State the blood parasite species.
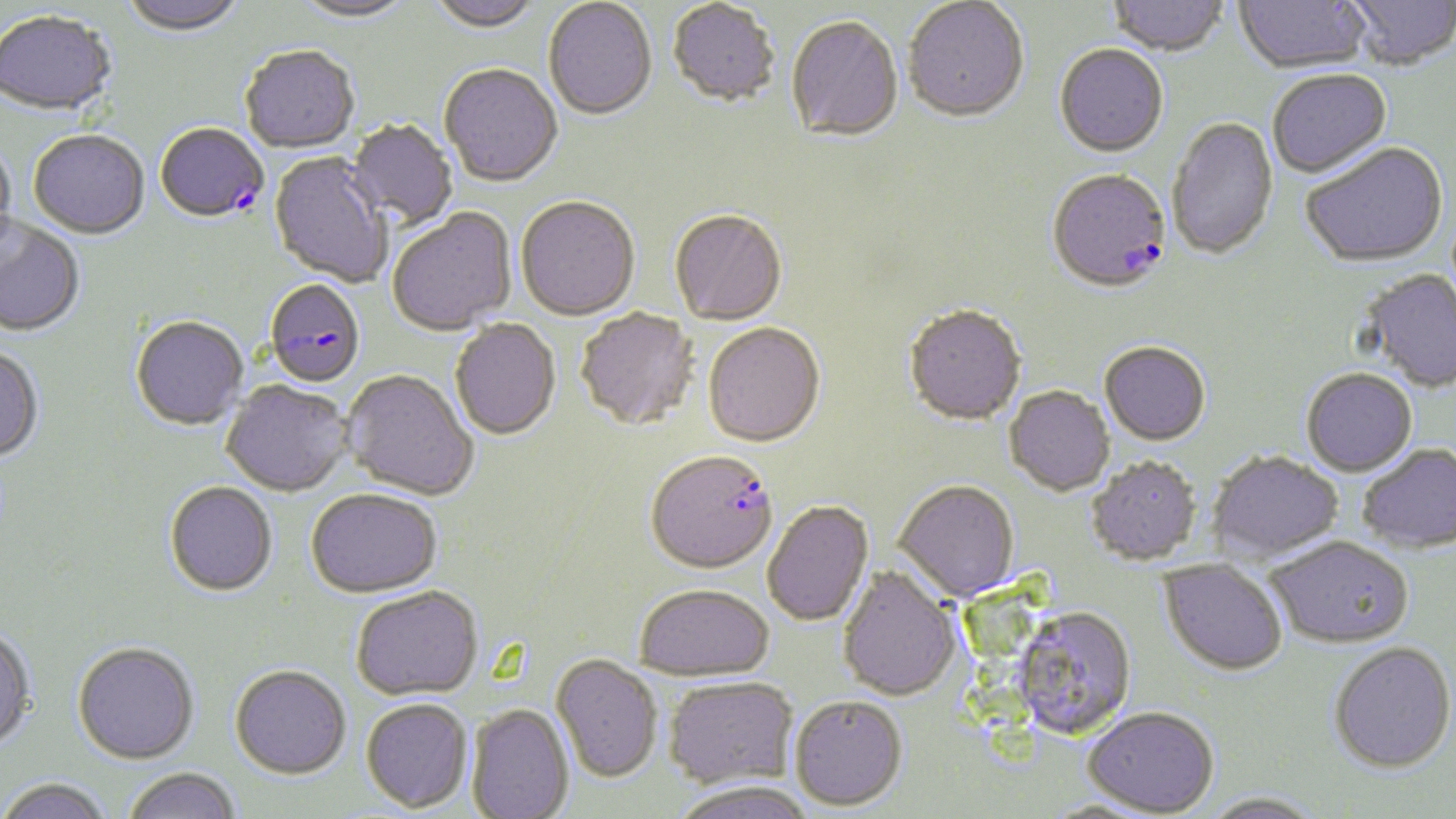
Plasmodium falciparum.

stain = May-Grünwald-Giemsa
Plasmodium falciparum-infected red blood cell locations = approximate bounding boxes as named x1/y1/x2/y2 corners in pixels: (x1=155, y1=125, x2=269, y2=225), (x1=1047, y1=171, x2=1172, y2=296), (x1=264, y1=281, x2=365, y2=389), (x1=646, y1=452, x2=779, y2=576)
magnification = 1000x
image size = 1456×819 pixels
modality = optical microscopy
preparation = thin blood smear
field of view = single
uninfected red blood cell locations = approximate bounding boxes as named x1/y1/x2/y2 corners in pixels: (x1=118, y1=0, x2=248, y2=38), (x1=291, y1=0, x2=418, y2=26), (x1=426, y1=0, x2=544, y2=36), (x1=1234, y1=0, x2=1372, y2=75), (x1=1342, y1=0, x2=1456, y2=73), (x1=543, y1=1, x2=657, y2=123), (x1=903, y1=1, x2=1029, y2=125), (x1=1107, y1=1, x2=1228, y2=58), (x1=667, y1=2, x2=780, y2=110), (x1=0, y1=13, x2=117, y2=120), (x1=786, y1=18, x2=904, y2=145), (x1=1054, y1=46, x2=1168, y2=159), (x1=240, y1=47, x2=360, y2=155), (x1=438, y1=65, x2=563, y2=189), (x1=1267, y1=71, x2=1392, y2=180), (x1=1167, y1=118, x2=1279, y2=262), (x1=347, y1=119, x2=458, y2=230), (x1=28, y1=132, x2=149, y2=241), (x1=0, y1=139, x2=17, y2=256), (x1=1301, y1=145, x2=1449, y2=270), (x1=267, y1=154, x2=392, y2=288), (x1=515, y1=198, x2=640, y2=322), (x1=388, y1=209, x2=517, y2=336), (x1=669, y1=212, x2=787, y2=327), (x1=0, y1=218, x2=85, y2=339), (x1=1360, y1=270, x2=1456, y2=393), (x1=904, y1=307, x2=1026, y2=428), (x1=575, y1=309, x2=700, y2=433), (x1=129, y1=316, x2=249, y2=431), (x1=450, y1=320, x2=561, y2=442), (x1=703, y1=324, x2=826, y2=449), (x1=1099, y1=343, x2=1211, y2=447), (x1=0, y1=347, x2=45, y2=465), (x1=1300, y1=369, x2=1418, y2=477), (x1=341, y1=371, x2=478, y2=501), (x1=221, y1=381, x2=353, y2=497), (x1=1004, y1=386, x2=1115, y2=497), (x1=1357, y1=443, x2=1456, y2=553), (x1=1207, y1=450, x2=1344, y2=563), (x1=1086, y1=457, x2=1202, y2=565), (x1=894, y1=480, x2=1020, y2=603), (x1=164, y1=481, x2=278, y2=597), (x1=305, y1=489, x2=442, y2=598), (x1=763, y1=500, x2=874, y2=626), (x1=1267, y1=535, x2=1414, y2=649), (x1=1158, y1=560, x2=1288, y2=676), (x1=837, y1=566, x2=962, y2=701), (x1=635, y1=583, x2=774, y2=681), (x1=351, y1=586, x2=483, y2=700), (x1=1012, y1=608, x2=1137, y2=740), (x1=0, y1=627, x2=36, y2=753), (x1=72, y1=641, x2=199, y2=764), (x1=1327, y1=642, x2=1456, y2=773), (x1=551, y1=654, x2=662, y2=784), (x1=229, y1=664, x2=351, y2=779), (x1=663, y1=676, x2=798, y2=790), (x1=788, y1=695, x2=907, y2=811), (x1=360, y1=698, x2=473, y2=813), (x1=466, y1=704, x2=574, y2=819), (x1=1082, y1=707, x2=1220, y2=817), (x1=122, y1=767, x2=242, y2=819), (x1=0, y1=778, x2=114, y2=819), (x1=671, y1=780, x2=817, y2=819), (x1=1200, y1=792, x2=1325, y2=818)